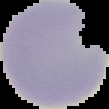
Cell region segmented out of the field of view; the surrounding area is masked to black. Malaria status: uninfected. Image is 109×109 pixels. From a thin blood film.